Comment on the morphology of the erythrocytes.
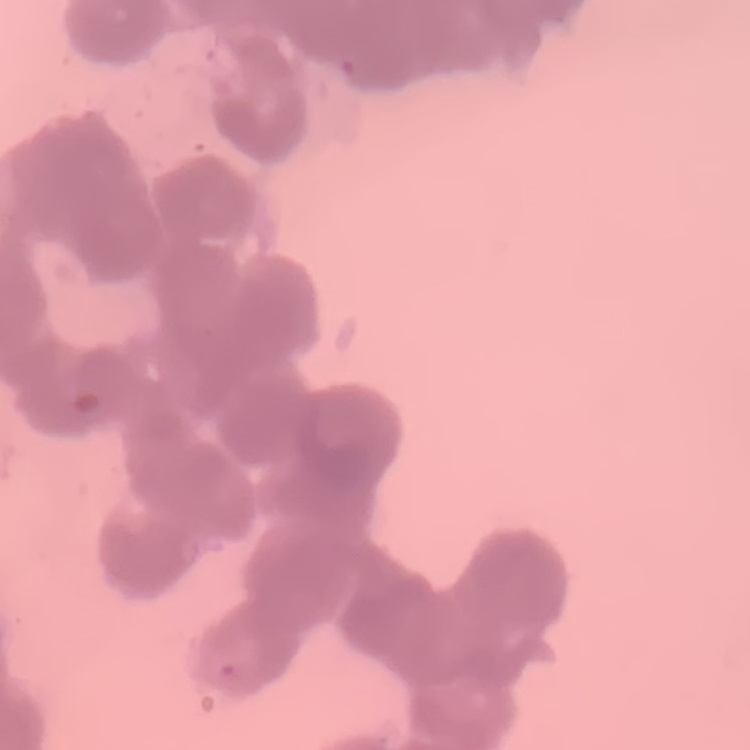

Rouleaux formation.

Summary:
  - Stain: Field's or Giemsa
  - Image type: square crop of a larger photomicrograph
  - Preparation: thin peripheral smear